State which parasite is depicted.
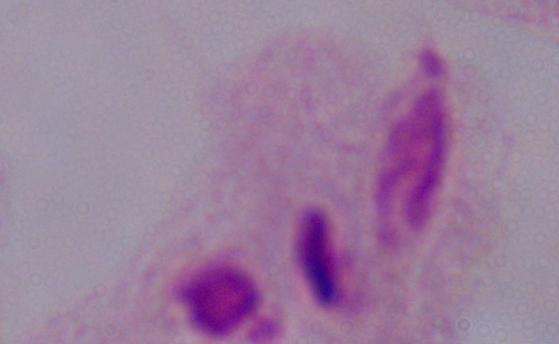
A trichomonad.

modality = micrograph
magnification = 1000x